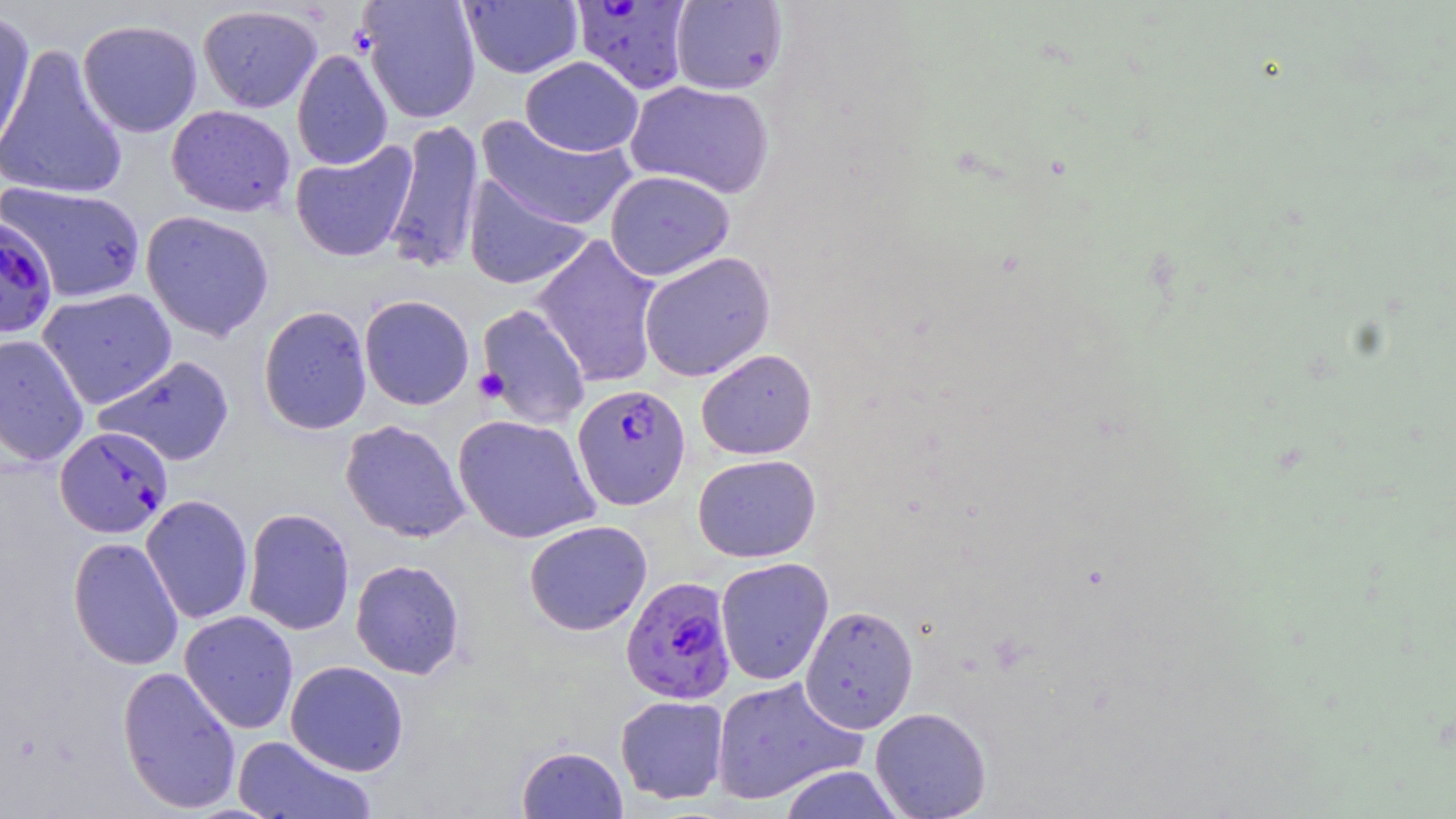
Summary:
  - Coordinate format: approximate bounding boxes as named x1/y1/x2/y2 corners in pixels
  - Uninfected red blood cell locations: (x1=358, y1=0, x2=481, y2=123), (x1=459, y1=1, x2=584, y2=78), (x1=669, y1=1, x2=788, y2=95), (x1=198, y1=4, x2=322, y2=113), (x1=0, y1=9, x2=36, y2=159), (x1=77, y1=19, x2=202, y2=138), (x1=0, y1=42, x2=128, y2=202), (x1=292, y1=48, x2=393, y2=171), (x1=520, y1=56, x2=644, y2=157), (x1=625, y1=80, x2=775, y2=199), (x1=167, y1=105, x2=296, y2=217), (x1=475, y1=115, x2=637, y2=232), (x1=383, y1=117, x2=484, y2=275), (x1=290, y1=141, x2=418, y2=263), (x1=604, y1=170, x2=734, y2=280), (x1=463, y1=175, x2=592, y2=290), (x1=1, y1=182, x2=147, y2=302), (x1=140, y1=210, x2=275, y2=341), (x1=532, y1=234, x2=664, y2=388), (x1=638, y1=251, x2=775, y2=382), (x1=37, y1=288, x2=178, y2=409), (x1=359, y1=295, x2=475, y2=410), (x1=475, y1=303, x2=592, y2=430), (x1=258, y1=305, x2=373, y2=435), (x1=0, y1=334, x2=90, y2=467), (x1=696, y1=348, x2=817, y2=460), (x1=93, y1=354, x2=235, y2=466), (x1=452, y1=414, x2=601, y2=544), (x1=340, y1=419, x2=471, y2=543), (x1=692, y1=454, x2=822, y2=562), (x1=140, y1=494, x2=254, y2=624), (x1=242, y1=507, x2=355, y2=636), (x1=524, y1=520, x2=652, y2=636), (x1=67, y1=536, x2=184, y2=671), (x1=715, y1=557, x2=834, y2=686), (x1=350, y1=559, x2=466, y2=680), (x1=799, y1=605, x2=919, y2=733), (x1=179, y1=610, x2=299, y2=734), (x1=285, y1=661, x2=409, y2=776), (x1=117, y1=666, x2=241, y2=814), (x1=711, y1=676, x2=866, y2=806), (x1=615, y1=695, x2=729, y2=804), (x1=870, y1=707, x2=992, y2=819), (x1=232, y1=735, x2=375, y2=819), (x1=516, y1=745, x2=628, y2=818), (x1=777, y1=764, x2=905, y2=819)
  - Plasmodium falciparum-infected red blood cell locations: (x1=569, y1=1, x2=695, y2=96), (x1=0, y1=216, x2=59, y2=339), (x1=572, y1=384, x2=690, y2=510), (x1=54, y1=425, x2=173, y2=538), (x1=621, y1=576, x2=736, y2=705)
  - Platelet locations: (x1=473, y1=368, x2=509, y2=403)
  - Slide-level diagnosis: Plasmodium falciparum
  - Image size: 1456×819 pixels
  - Magnification: 1000x
  - Modality: light microscopy
  - Preparation: thin blood smear
  - Stain: May-Grünwald-Giemsa
  - Field of view: single